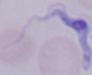
Micrograph. 1000x magnification. A trypanosome is shown.